Locate every leukocyte (white blood cell).
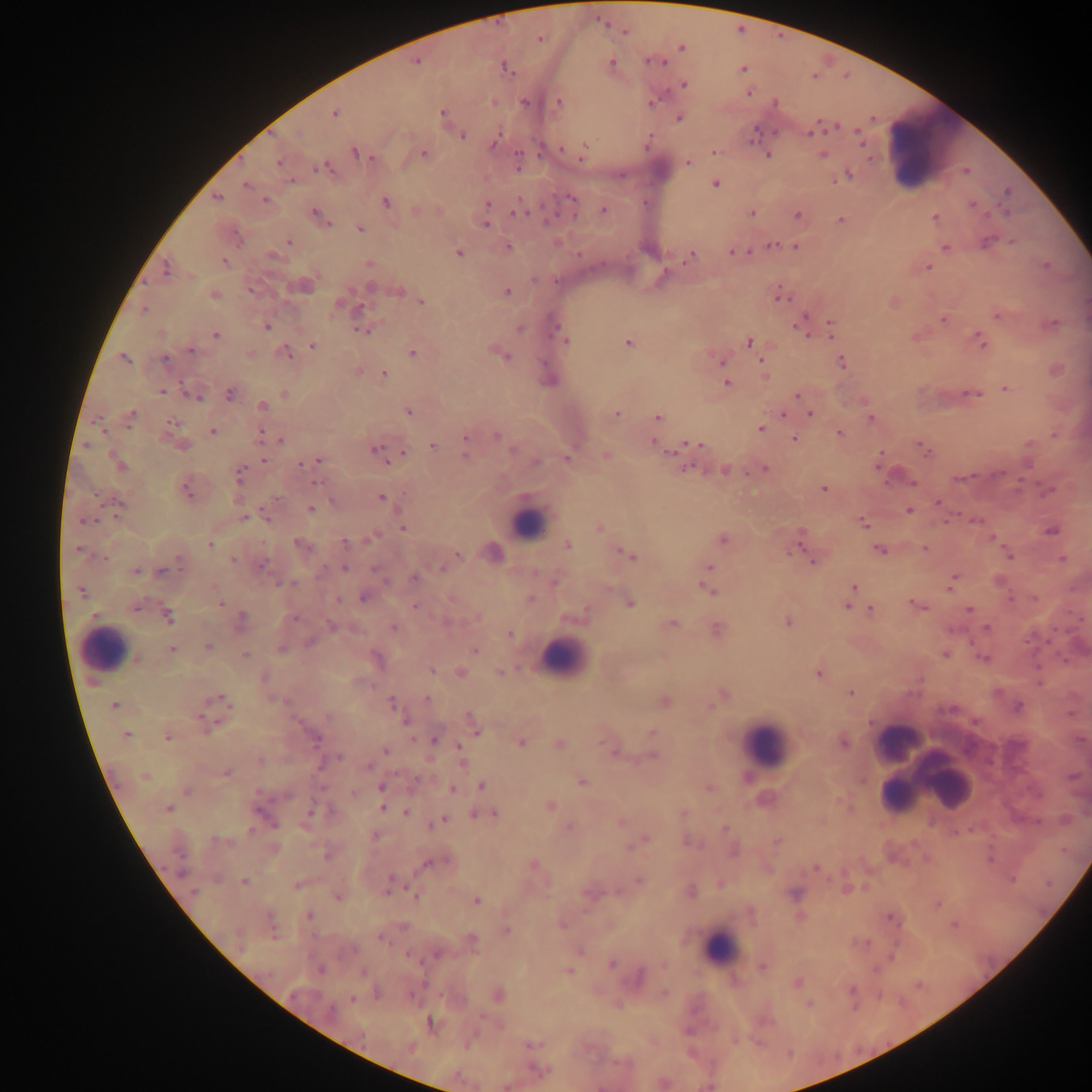

Approximate centers as x y in pixels.
Leukocytes: 933 151; 528 522; 106 650; 562 658; 898 741; 767 744; 910 756; 936 774; 899 795; 720 948.

capture = mobile-phone photograph through a microscope
Plasmodium parasite locations = approximate centers as x y in pixels: 626 32; 540 39; 681 48; 416 61; 611 62; 654 62; 506 68; 742 69; 684 84; 748 92; 525 102; 560 102; 652 102; 776 103; 335 113; 442 113; 679 117; 811 131; 858 132; 463 136; 494 143; 585 147; 714 151; 356 153; 424 154; 767 156; 823 156; 279 162; 688 163; 518 165; 325 168; 966 171; 849 175; 292 182; 245 184; 715 184; 1007 191; 216 198; 572 199; 265 200; 385 202; 487 203; 973 204; 603 210; 520 211; 751 212; 1006 213; 316 214; 797 214; 935 218; 841 219; 485 225; 360 229; 987 241; 289 242; 772 245; 795 246; 507 247; 945 247; 458 253; 734 253; 692 256; 225 262; 369 264; 1046 266; 928 267; 166 270; 662 278; 304 286; 370 287; 400 290; 251 291; 507 292; 214 294; 781 296; 422 302; 338 303; 361 307; 143 309; 997 316; 943 320; 831 323; 1052 323; 267 326; 800 326; 556 328; 521 329; 362 331; 804 332; 216 334; 560 335; 565 341; 980 341; 628 342; 749 342; 312 346; 191 351; 285 352; 412 353; 506 357; 124 359; 165 359; 722 362; 842 362; 762 364; 764 373; 383 374; 727 383; 1006 388; 162 391; 230 393; 284 394; 973 394; 797 395; 195 397; 263 406; 409 412; 617 414; 783 414; 810 414; 130 417; 658 417; 871 418; 172 423; 760 429; 212 430; 840 433; 259 434; 496 436; 465 437; 794 439; 280 441; 653 443; 694 443; 1029 444; 432 445; 183 446; 922 448; 375 449; 513 449; 402 453; 465 456; 607 456; 567 459; 263 460; 318 460; 536 462; 302 463; 119 465; 687 468; 764 469; 725 470; 239 475; 962 478; 315 483; 912 483; 824 489; 187 490; 381 497; 938 502; 119 504; 310 509; 908 511; 243 518; 267 518; 974 520; 83 521; 864 524; 402 526; 599 528; 1051 531; 801 534; 372 537; 723 539; 345 542; 299 544; 210 545; 567 545; 924 548; 878 549; 77 550; 493 551; 791 551; 457 555; 628 556; 1009 556; 103 558; 1062 559; 233 560; 813 560; 180 561; 262 564; 709 567; 344 568; 442 569; 376 570; 136 571; 161 572; 414 578; 556 580; 952 581; 998 581; 291 584; 853 587; 707 589; 81 592; 362 598; 530 599; 338 600; 221 603; 630 604; 917 605; 847 606; 136 607; 415 607; 969 608; 872 609; 168 617; 478 617; 294 618; 241 620; 788 622; 672 623; 332 626; 986 627; 393 628; 717 630; 510 634; 310 642; 208 647; 280 648; 172 649; 475 649; 245 655; 945 655; 983 658; 136 659; 377 659; 431 670; 460 672; 500 672; 818 674; 851 693; 723 694; 427 698; 221 699; 391 702; 665 702; 114 705; 1018 707; 328 716; 405 720; 206 721; 472 722; 476 730; 651 732; 126 736; 167 738; 316 738; 435 740; 522 743; 559 743; 843 743; 459 746; 385 750; 652 756; 340 757; 261 761; 462 763; 369 767; 225 773; 144 777; 582 782; 482 786; 381 788; 709 788; 452 789; 187 792; 287 796; 550 805; 168 808; 382 809; 311 812; 406 812; 683 813; 477 814; 493 814; 442 820; 620 822; 436 823; 568 827; 725 828; 375 836; 214 840; 645 840; 778 841; 326 857; 429 864; 534 865; 815 868; 181 873; 639 880; 244 881; 296 885; 388 891; 691 891; 194 893; 795 894; 338 896; 415 897; 477 902; 938 905; 309 915; 891 918; 563 925; 506 929; 380 938; 472 939; 611 963; 763 967; 321 969; 567 971; 797 982; 851 990; 498 996; 352 999; 808 1004; 330 1011; 431 1022; 533 1043; 538 1070
field of view = single
preparation = thick blood smear
image size = 1092×1092 pixels
country = Ghana